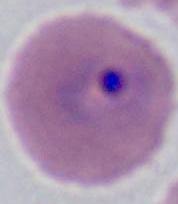
A Plasmodium parasite is seen. Captured at either 400x or 1000x magnification. Micrograph.